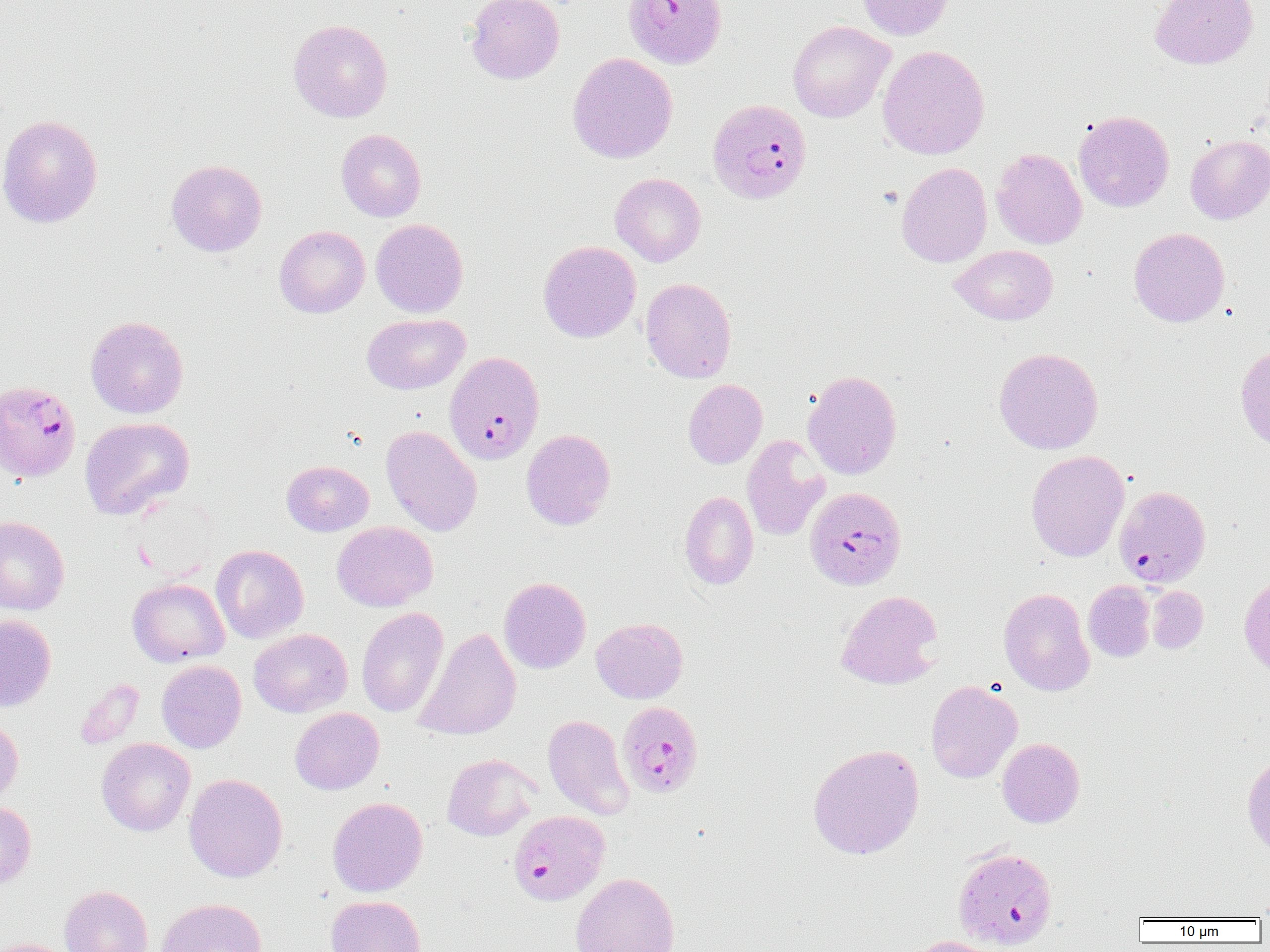

slide-level diagnosis = Plasmodium falciparum
field of view = single
image size = 1270×952 pixels
modality = optical microscopy
preparation = thin blood film
Plasmodium falciparum-infected red blood cell locations = approximate bounding boxes as (x1,y1)-(x2,y2) corner pairs in pixels: (622,0)-(727,69), (707,98)-(812,205), (445,351)-(544,464), (0,380)-(81,482), (805,486)-(906,590), (1114,486)-(1211,587), (617,700)-(704,799), (507,812)-(608,908)
uninfected red blood cell locations = approximate bounding boxes as (x1,y1)-(x2,y2) corner pairs in pixels: (465,0)-(564,84), (856,0)-(953,40), (1149,0)-(1258,69), (288,19)-(392,123), (788,20)-(895,123), (877,45)-(990,160), (567,52)-(678,163), (1074,110)-(1174,212), (0,114)-(103,228), (336,128)-(426,221), (1185,134)-(1270,224), (991,148)-(1087,249), (166,159)-(267,257), (898,159)-(1090,258), (896,162)-(992,267), (610,173)-(706,266), (371,219)-(468,318), (274,226)-(370,318), (1129,227)-(1230,327), (538,241)-(641,342), (950,245)-(1058,325), (640,277)-(737,383), (361,313)-(469,394), (85,315)-(189,418), (1235,344)-(1270,452), (994,347)-(1104,454), (802,370)-(902,479), (683,379)-(768,469), (80,417)-(194,520), (380,425)-(482,536), (521,429)-(615,530), (742,434)-(830,541), (1025,450)-(1130,562), (281,460)-(374,536), (679,491)-(759,590), (0,515)-(70,615), (331,521)-(438,611), (211,544)-(309,643), (1239,573)-(1270,680), (499,576)-(591,674), (127,577)-(229,667), (1083,581)-(1155,662), (1147,586)-(1208,654), (998,587)-(1095,696), (836,590)-(943,689), (356,607)-(448,718), (0,614)-(56,712), (591,617)-(688,703), (414,626)-(521,741), (249,628)-(352,717), (156,660)-(246,753), (75,679)-(145,749), (925,680)-(1022,783), (290,707)-(384,794), (542,714)-(634,819), (0,716)-(23,807), (96,738)-(195,836), (997,738)-(1085,828), (807,743)-(924,860), (442,753)-(540,841), (1242,753)-(1270,858), (183,773)-(288,882), (328,796)-(428,897), (0,800)-(36,891), (570,872)-(680,952), (59,885)-(154,952), (326,895)-(427,952), (156,897)-(267,952), (907,935)-(1007,952), (0,937)-(75,952)
magnification = 1000x